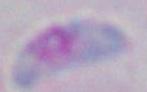
Toxoplasma gondii is shown. Captured at 1000x magnification. Photomicrograph.